Outline each uninfected red blood cell.
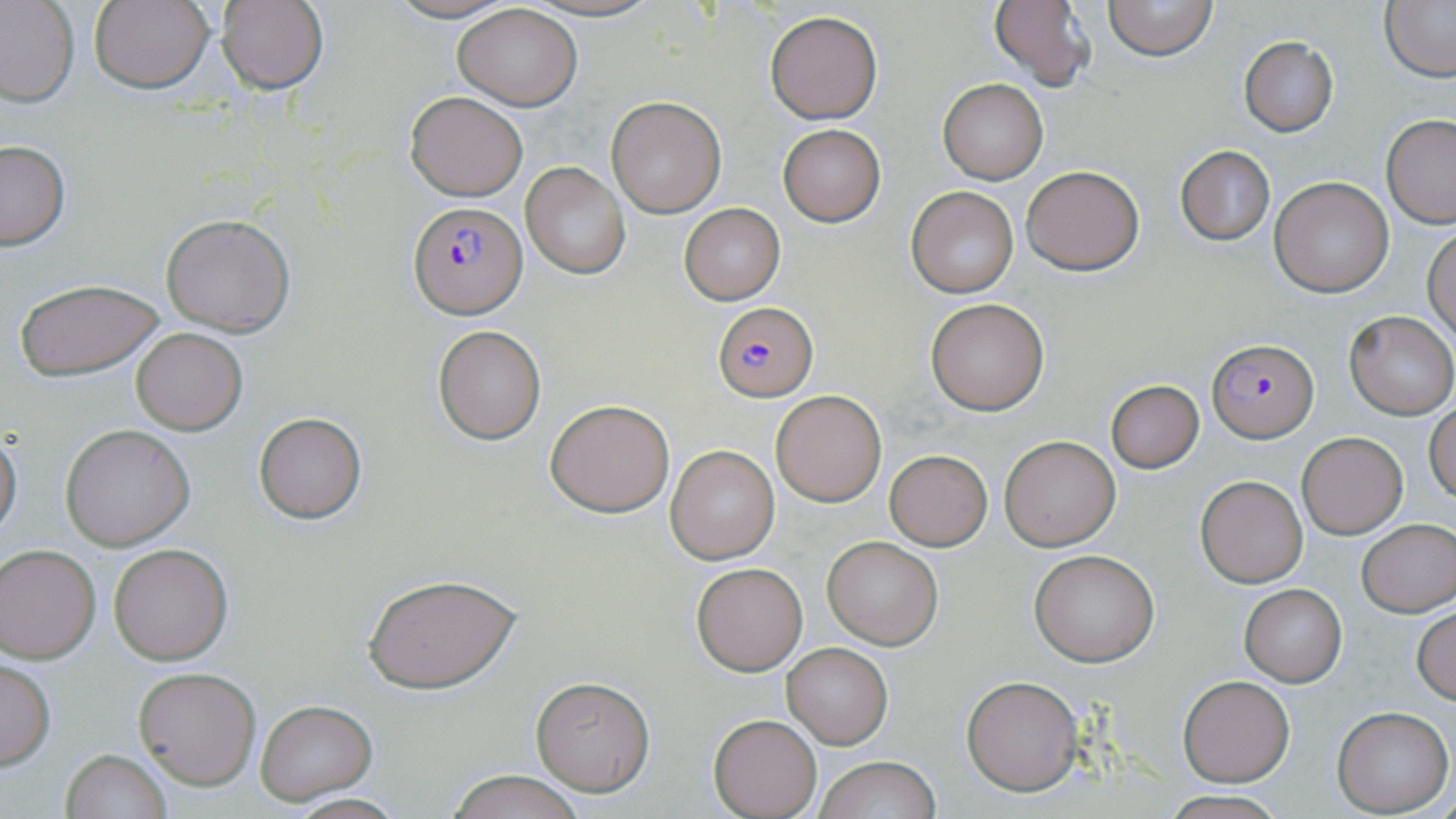

Approximate bounding boxes as [x1, y1, x2, y2] in pixels.
Uninfected red blood cells: [0, 0, 80, 106], [88, 0, 215, 93], [381, 0, 521, 23], [989, 0, 1095, 91], [1103, 0, 1217, 63], [1380, 0, 1456, 84], [213, 1, 330, 93], [452, 4, 583, 110], [765, 9, 883, 124], [1239, 37, 1338, 136], [937, 77, 1048, 184], [405, 91, 528, 200], [606, 95, 726, 218], [1380, 113, 1456, 227], [778, 124, 885, 226], [0, 141, 71, 251], [1175, 146, 1274, 246], [520, 163, 628, 279], [1021, 165, 1144, 275], [1269, 176, 1395, 296], [906, 186, 1019, 297], [679, 203, 784, 304], [161, 214, 295, 336], [1424, 227, 1456, 342], [17, 280, 164, 381], [925, 298, 1048, 415], [1344, 311, 1454, 419], [432, 324, 546, 444], [130, 326, 248, 436], [1105, 379, 1205, 473], [771, 390, 888, 507], [545, 398, 676, 518], [1426, 402, 1456, 504], [254, 412, 366, 523], [61, 425, 194, 551], [0, 431, 22, 538], [1297, 431, 1407, 538], [999, 434, 1121, 551], [667, 446, 779, 563], [885, 450, 992, 550], [1194, 474, 1308, 587], [1357, 519, 1456, 617], [822, 536, 942, 649], [108, 543, 232, 665], [0, 545, 101, 662], [1028, 549, 1159, 666], [692, 563, 807, 675], [364, 570, 522, 695], [1239, 583, 1347, 687], [1412, 606, 1456, 704], [781, 642, 893, 748], [0, 658, 56, 771], [134, 667, 260, 789], [530, 674, 656, 795], [961, 676, 1084, 794], [1177, 676, 1295, 786], [254, 699, 376, 803], [1331, 706, 1453, 816], [709, 714, 821, 818], [61, 749, 173, 819], [812, 756, 942, 819], [448, 770, 586, 819], [1156, 792, 1293, 819], [274, 793, 411, 819].

slide-level diagnosis = Plasmodium falciparum
preparation = thin blood film
Plasmodium falciparum-infected red blood cell locations = approximate bounding boxes as [x1, y1, x2, y2] in pixels: [410, 201, 526, 317], [713, 301, 818, 402], [1207, 338, 1317, 441]
image size = 1456×819 pixels
modality = optical microscopy
stain = May-Grünwald-Giemsa
magnification = 1000x
field of view = single